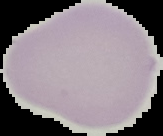
preparation = thin blood smear
image size = 163×136 pixels
result = negative for malaria parasites
image type = segmented cell region on a black background